Evaluate for Plasmodium parasites.
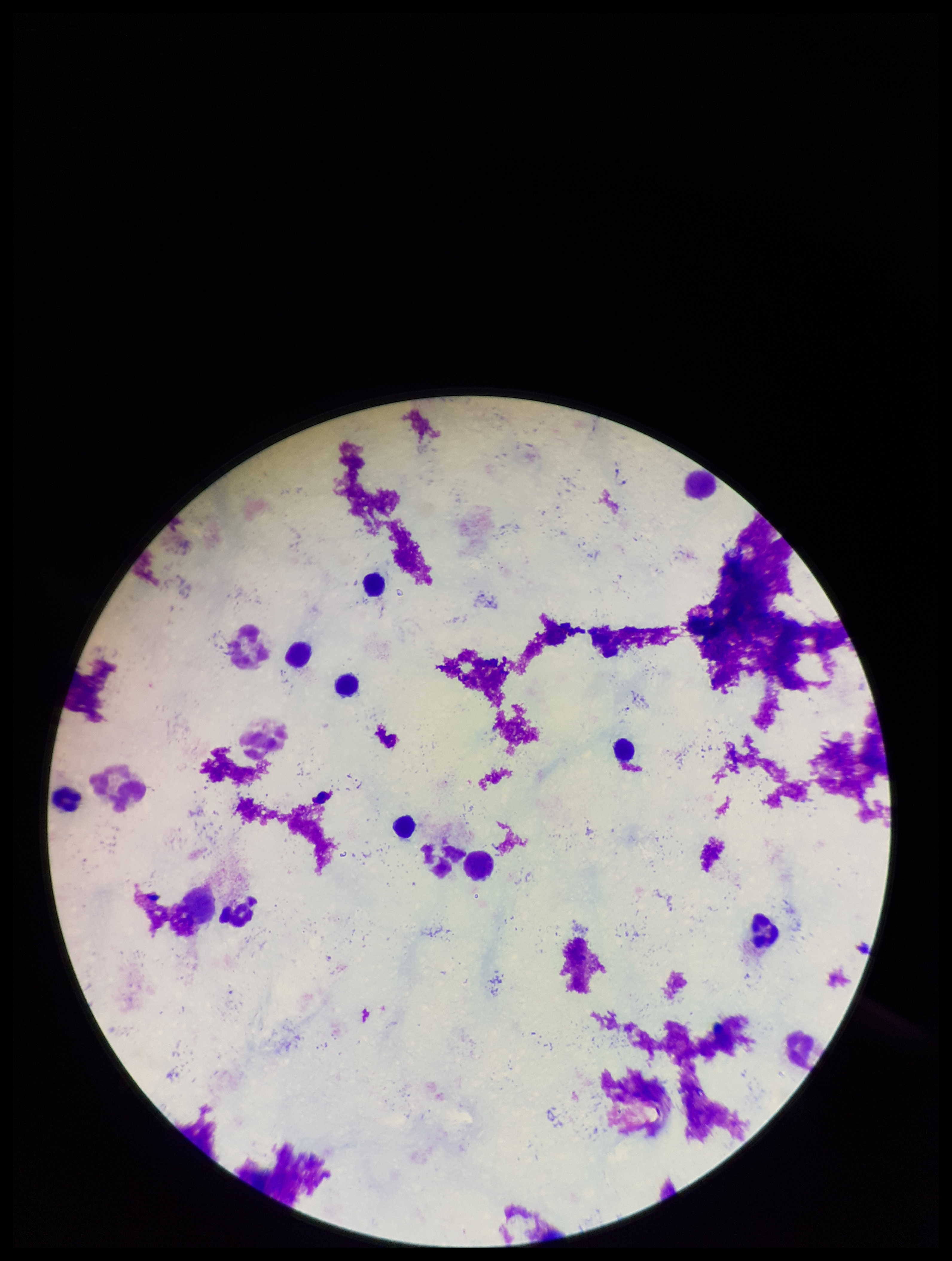
None detected.

preparation = thick
stain = Giemsa
patient malaria status = negative
leukocyte count = 10
field of view = single
image size = 952×1261 pixels
parasite count = 0
capture = smartphone photograph through the microscope eyepiece